State the blood parasite species.
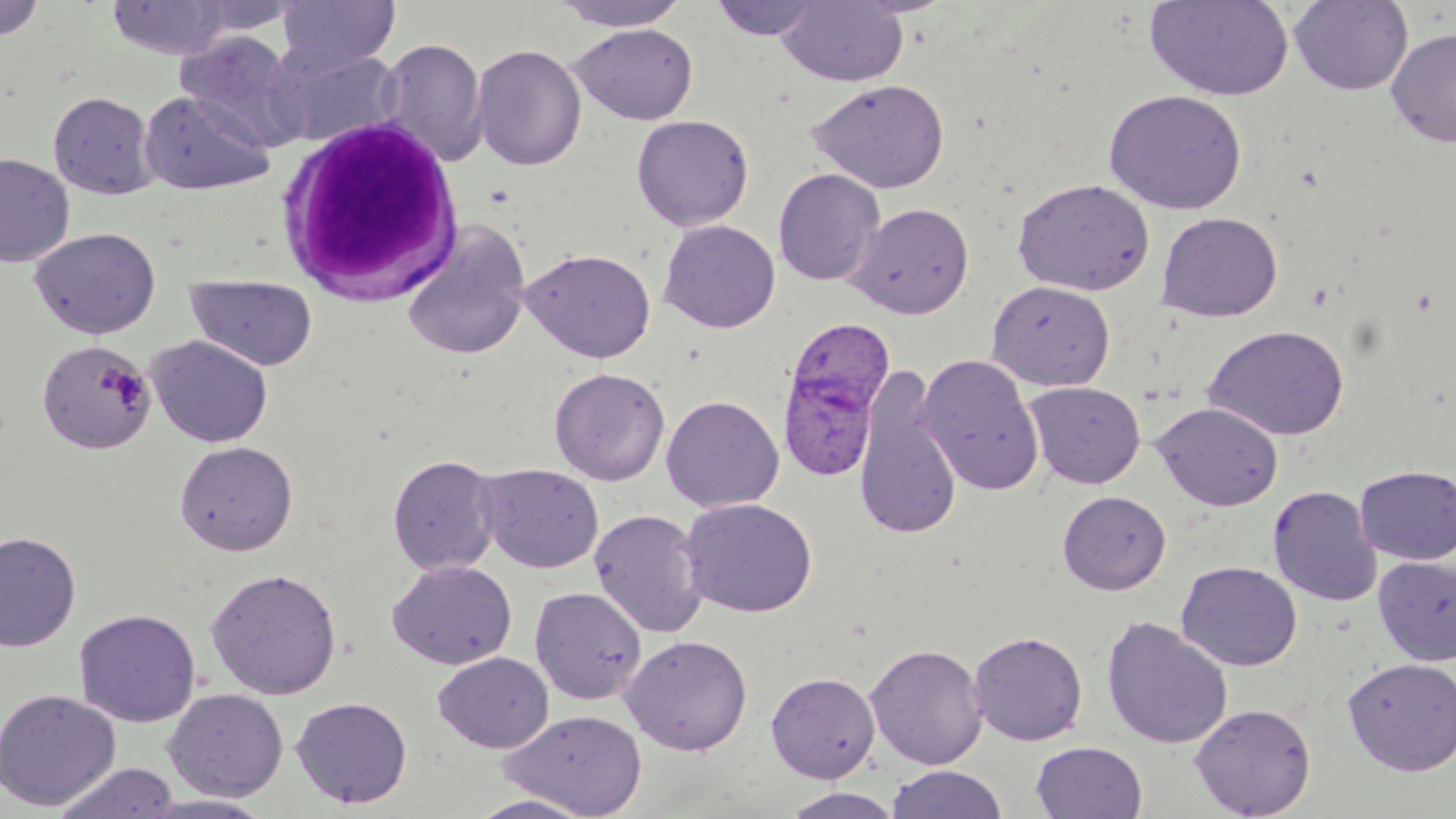
Plasmodium ovale.

white blood cell locations = approximate bounding boxes as (x1,y1)-(x2,y2) corner pairs in pixels: (273,112)-(466,306)
Plasmodium ovale-infected red blood cell locations = approximate bounding boxes as (x1,y1)-(x2,y2) corner pairs in pixels: (785,316)-(895,432), (777,359)-(882,486)
magnification = 1000x
preparation = thin blood film
uninfected red blood cell locations = approximate bounding boxes as (x1,y1)-(x2,y2) corner pairs in pixels: (107,0)-(230,59), (188,0)-(304,37), (277,0)-(399,73), (550,0)-(692,31), (709,0)-(826,41), (776,0)-(908,87), (1144,0)-(1295,102), (1289,0)-(1414,95), (0,1)-(46,41), (570,23)-(698,125), (1386,26)-(1456,148), (174,31)-(303,147), (378,37)-(489,167), (472,43)-(586,171), (268,45)-(405,147), (807,79)-(950,193), (139,88)-(275,196), (1104,89)-(1247,214), (49,91)-(156,199), (631,114)-(754,231), (0,152)-(74,268), (773,168)-(886,286), (1012,178)-(1155,295), (846,202)-(974,319), (1156,211)-(1283,322), (658,219)-(780,333), (29,226)-(161,339), (400,226)-(533,361), (518,247)-(656,363), (185,274)-(318,371), (986,279)-(1115,391), (1203,324)-(1350,441), (146,335)-(273,448), (37,339)-(154,454), (915,354)-(1045,495), (853,365)-(963,543), (549,367)-(670,485), (1024,380)-(1145,488), (661,394)-(785,512), (1152,402)-(1284,511), (175,440)-(298,556), (387,453)-(501,576), (477,463)-(604,573), (1355,464)-(1456,565), (1267,485)-(1382,607), (1057,490)-(1171,594), (679,497)-(818,618), (589,508)-(708,638), (0,531)-(81,652), (1373,556)-(1456,666), (387,560)-(517,669), (1175,560)-(1302,672), (205,568)-(342,699), (529,585)-(648,705), (74,608)-(201,727), (1101,615)-(1233,749), (969,630)-(1088,745), (621,634)-(753,755), (864,642)-(987,769), (433,652)-(554,753), (1342,657)-(1456,775), (766,672)-(880,782), (0,688)-(121,811), (163,688)-(288,801), (291,696)-(413,808), (1189,702)-(1316,818), (500,708)-(647,818), (1031,741)-(1148,819), (51,762)-(181,819), (886,765)-(1008,818), (780,787)-(905,818), (137,793)-(278,818), (465,793)-(602,818)
modality = light microscopy
stain = May-Grünwald-Giemsa
image size = 1456×819 pixels
field of view = one of a larger specimen